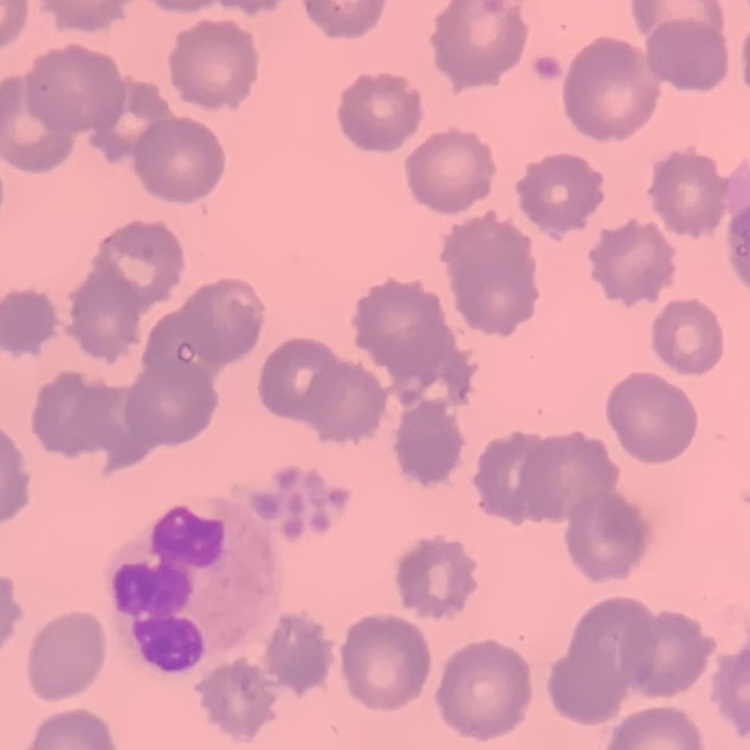
erythrocyte morphology = no rouleaux formation
image type = square crop of a larger photomicrograph
stain = Field's or Giemsa
preparation = thin blood film